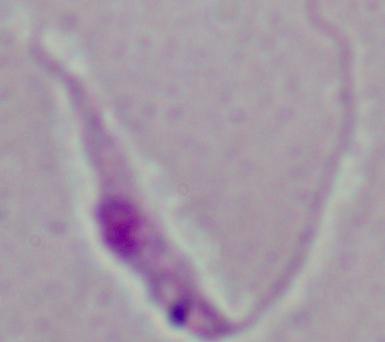
A Leishmania parasite is seen. Captured at 1000x magnification. Micrograph.